Locate every Plasmodium parasite and every leukocyte.
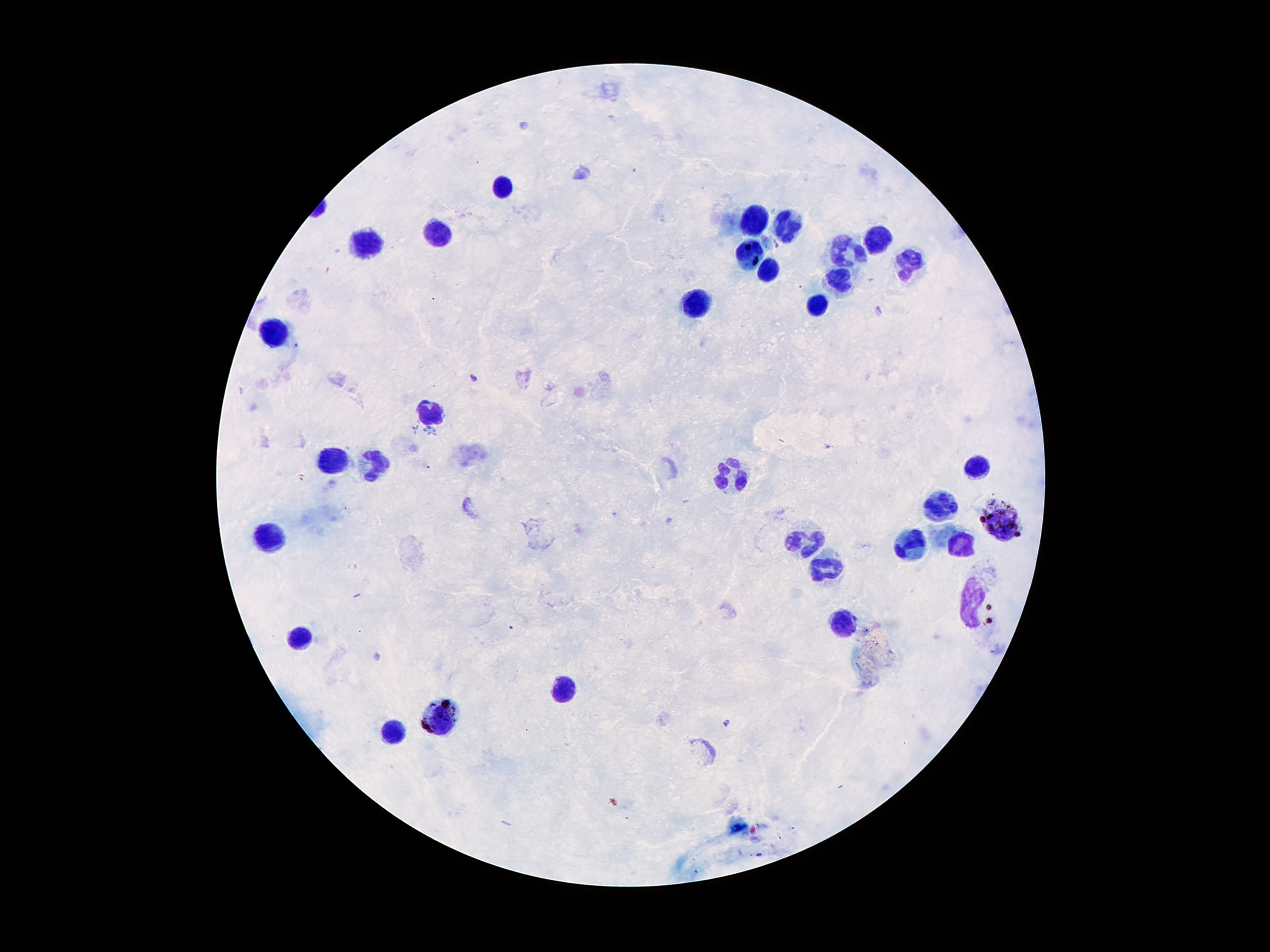
Approximate centers as {x, y} in pixels.
Plasmodium parasites: {880, 311}, {474, 377}, {414, 430}, {430, 432}, {828, 447}, {725, 722}.
Leukocytes: {503, 187}, {757, 215}, {786, 226}, {443, 233}, {877, 237}, {364, 245}, {843, 255}, {748, 257}, {909, 263}, {770, 273}, {836, 282}, {696, 303}, {818, 307}, {275, 335}, {428, 411}, {334, 460}, {373, 464}, {975, 467}, {725, 474}, {938, 506}, {1004, 520}, {273, 537}, {804, 542}, {963, 548}, {909, 551}, {825, 571}, {968, 595}, {843, 621}, {298, 635}, {560, 690}, {441, 719}, {394, 734}.

Smartphone photograph taken through the microscope eyepiece. One field from this slide. Image is 1270×952 pixels. Giemsa stain. Patient malaria status: positive for Plasmodium falciparum. Thick peripheral-blood smear. 100x magnification.